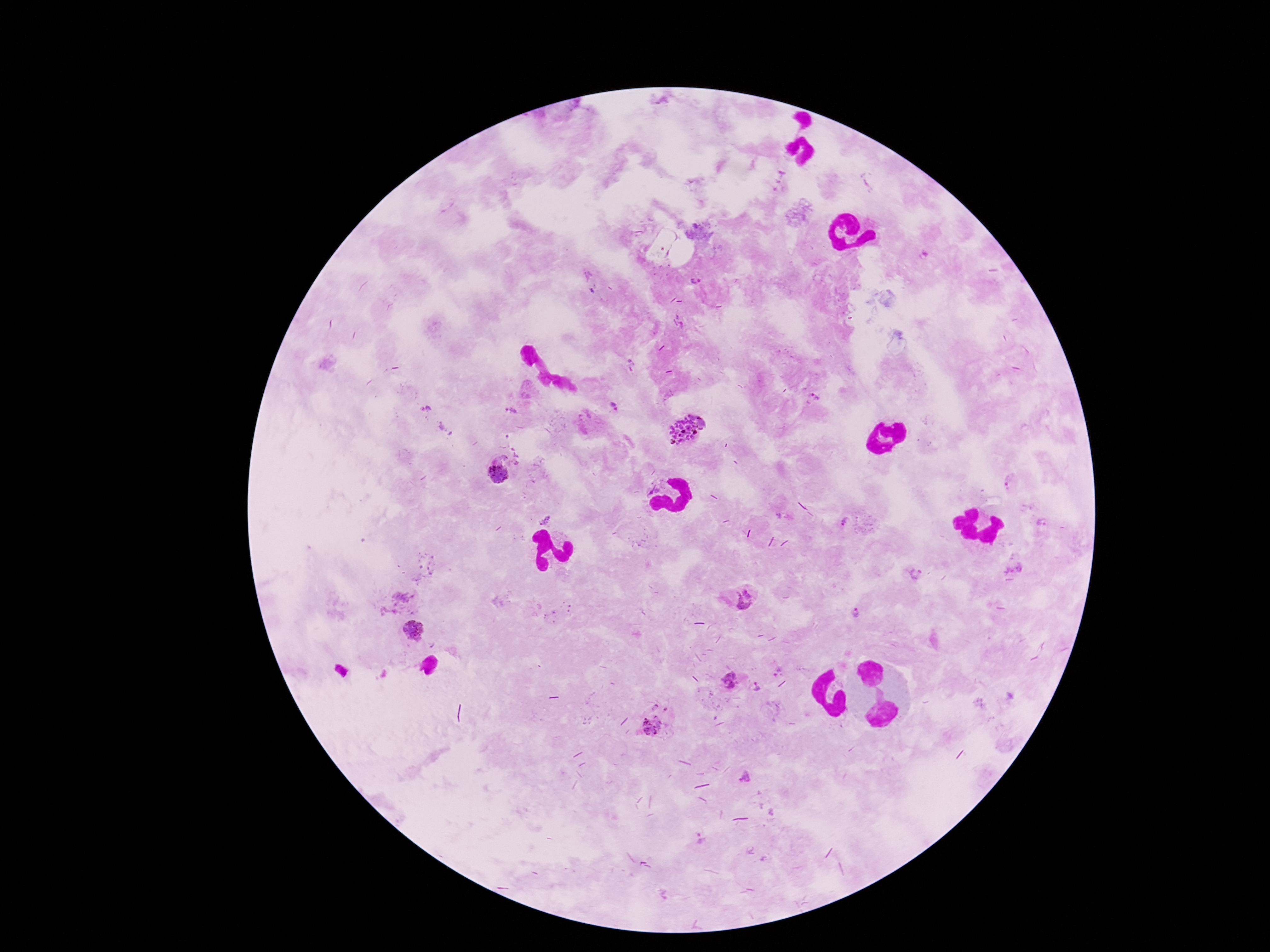
Approximate centers as (x, y) in pixels.
Summary:
  - Plasmodium parasite locations: (695, 282), (814, 399), (614, 408), (511, 411), (692, 414), (703, 420), (683, 432), (513, 449), (517, 455), (516, 463), (501, 473), (1011, 483), (546, 519), (843, 521), (1043, 523), (1016, 570), (917, 574), (743, 598), (858, 614), (414, 630), (730, 681), (756, 687), (655, 707), (665, 710), (653, 727), (747, 780), (700, 840)
  - Field of view: single
  - Magnification: 100x
  - Capture: smartphone camera through the microscope eyepiece
  - Stain: Giemsa
  - Patient malaria status: positive
  - Image size: 1270×952 pixels
  - Preparation: thick blood film